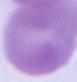
Photomicrograph. A red blood cell is shown. 1000x magnification.